Report the malaria status of this cell.
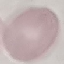
Uninfected.

Summary:
  - Preparation: thin blood smear
  - Image type: cell patch, automatically extracted from a larger field of view and resized to 64 × 64 pixels
  - Capture: smartphone camera at the microscope eyepiece
  - Stain: Giemsa